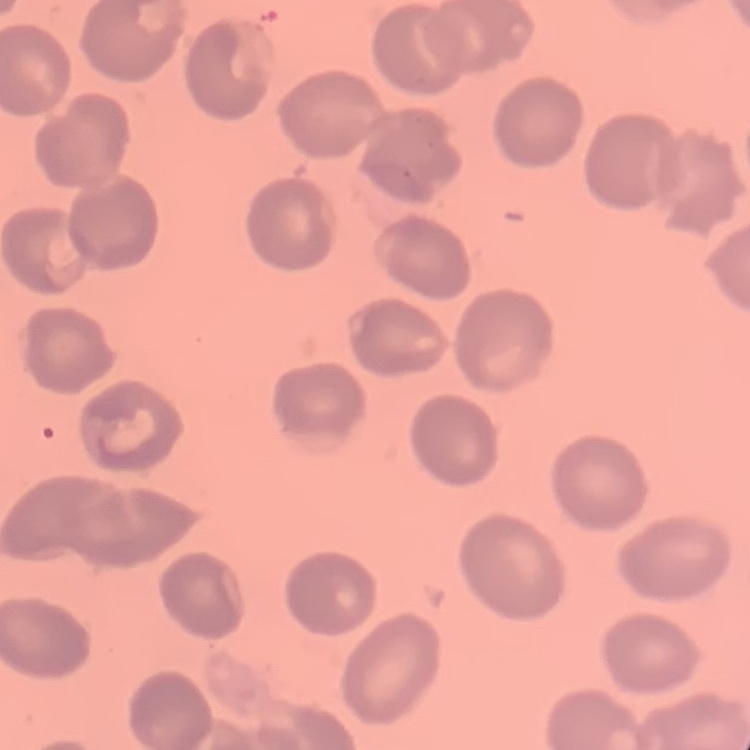

erythrocyte morphology = no rouleaux formation
preparation = thin blood smear
stain = Field's or Giemsa
image type = one tile cut from a larger photomicrograph